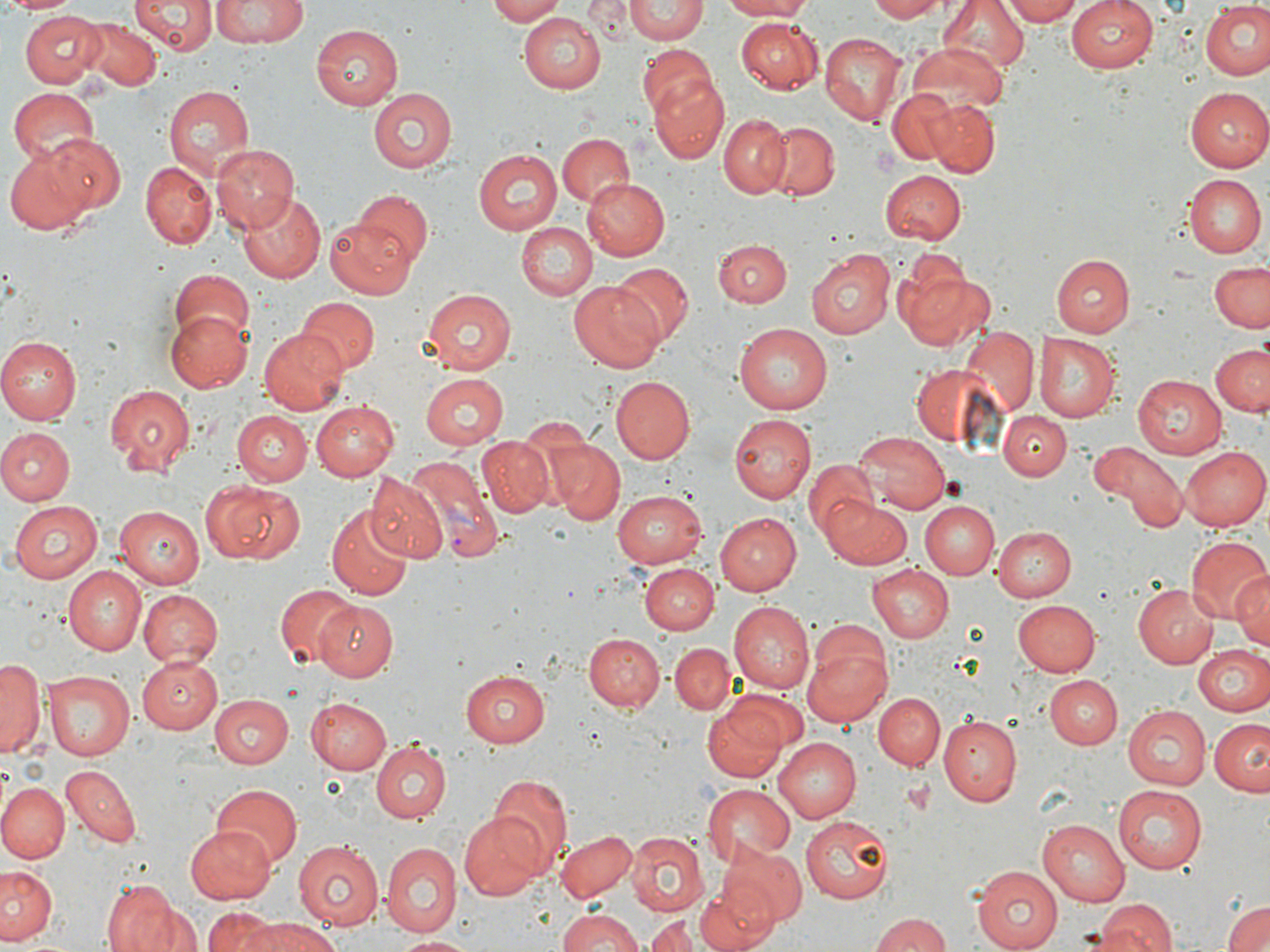

{
  "plasmodium_vivax_infected_red_blood_cell_locations": "approximate bounding boxes as [x1, y1, x2, y2] in pixels: [401, 456, 504, 563]",
  "slide_level_diagnosis": "Plasmodium vivax",
  "uninfected_red_blood_cell_locations": "approximate bounding boxes as [x1, y1, x2, y2] in pixels: [9, 0, 74, 16], [130, 0, 214, 55], [211, 0, 310, 46], [487, 0, 569, 24], [584, 0, 635, 41], [626, 0, 708, 44], [719, 0, 818, 20], [866, 0, 950, 21], [938, 0, 1029, 74], [999, 0, 1085, 25], [1067, 0, 1160, 73], [1201, 2, 1270, 80], [19, 11, 105, 88], [520, 12, 607, 94], [77, 15, 161, 92], [735, 17, 821, 92], [310, 24, 404, 109], [819, 33, 906, 127], [638, 44, 716, 120], [908, 45, 1009, 119], [648, 74, 731, 164], [162, 83, 255, 178], [8, 87, 102, 167], [886, 87, 965, 166], [1185, 87, 1270, 172], [367, 88, 454, 174], [922, 100, 999, 176], [718, 112, 791, 195], [765, 121, 839, 200], [556, 132, 634, 209], [39, 135, 124, 221], [211, 143, 299, 233], [5, 147, 94, 236], [473, 149, 562, 235], [139, 161, 216, 249], [882, 171, 967, 244], [1187, 174, 1265, 258], [584, 180, 672, 263], [357, 189, 433, 267], [236, 193, 327, 284], [327, 214, 416, 297], [518, 221, 597, 300], [714, 240, 791, 308], [807, 246, 895, 339], [891, 254, 992, 352], [1052, 254, 1135, 338], [1209, 260, 1270, 332], [612, 262, 693, 346], [170, 272, 254, 352], [570, 280, 666, 371], [421, 288, 515, 375], [297, 297, 379, 376], [165, 312, 252, 393], [735, 323, 834, 414], [259, 326, 349, 415], [959, 329, 1039, 419], [1034, 333, 1121, 422], [0, 336, 83, 423], [1209, 342, 1270, 418], [910, 363, 1005, 449], [420, 372, 509, 450], [1132, 374, 1226, 460], [613, 376, 695, 462], [104, 383, 195, 477], [310, 401, 398, 481], [234, 410, 311, 486], [1000, 411, 1071, 481], [729, 414, 814, 502], [0, 428, 74, 504], [856, 433, 950, 514], [476, 438, 552, 518], [548, 440, 624, 522], [1092, 443, 1187, 531], [1180, 445, 1270, 529], [802, 457, 880, 541], [366, 474, 447, 563], [199, 479, 302, 566], [614, 489, 709, 564], [821, 496, 911, 568], [9, 500, 103, 584], [918, 500, 999, 579], [329, 503, 411, 597], [117, 504, 205, 589], [714, 513, 801, 596], [995, 526, 1077, 603], [1186, 536, 1270, 625], [641, 563, 718, 636], [868, 563, 954, 643], [61, 566, 145, 655], [1232, 573, 1270, 651], [273, 582, 359, 669], [1136, 582, 1220, 668], [138, 589, 223, 666], [1011, 599, 1101, 677], [313, 600, 398, 680], [728, 601, 814, 694], [583, 633, 665, 712], [803, 633, 892, 726], [667, 641, 735, 714], [1192, 644, 1270, 715], [137, 657, 222, 734], [1, 659, 42, 756], [460, 669, 553, 747], [44, 670, 135, 760], [1046, 673, 1122, 747], [872, 691, 945, 770], [703, 692, 795, 783], [209, 694, 293, 769], [308, 696, 393, 773], [1122, 704, 1213, 788], [937, 716, 1022, 805], [1209, 717, 1270, 795], [773, 736, 861, 820], [372, 741, 450, 823], [62, 765, 141, 847], [489, 776, 572, 872], [0, 782, 68, 864], [210, 783, 303, 864], [701, 783, 797, 867], [1113, 785, 1208, 874], [457, 813, 551, 898], [802, 816, 894, 904], [1038, 819, 1130, 905], [184, 823, 276, 903], [554, 829, 636, 902], [627, 831, 709, 915], [292, 839, 386, 930], [380, 841, 463, 935], [720, 845, 806, 925], [1, 866, 59, 944], [971, 867, 1061, 951], [694, 880, 781, 952], [100, 883, 187, 952], [1095, 901, 1175, 952], [1222, 901, 1270, 952], [201, 907, 279, 952], [556, 908, 646, 952], [871, 913, 955, 952], [643, 916, 705, 951], [247, 918, 337, 952], [398, 935, 477, 951]",
  "image_size": "1270×952 pixels",
  "platelet_locations": "approximate bounding boxes as [x1, y1, x2, y2] in pixels: [870, 147, 900, 176]",
  "modality": "optical microscopy",
  "field_of_view": "one of a larger specimen",
  "magnification": "1000x",
  "preparation": "thin blood smear",
  "stain": "May-Grünwald-Giemsa"
}